Classify this cell by malaria status.
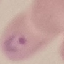
Parasitized.

Summary:
  - Stain: Giemsa
  - Capture: smartphone camera at the microscope eyepiece
  - Image type: automatically extracted cell patch, resized to 64 × 64 pixels
  - Preparation: thin blood film